Comment on the morphology of the red blood cells.
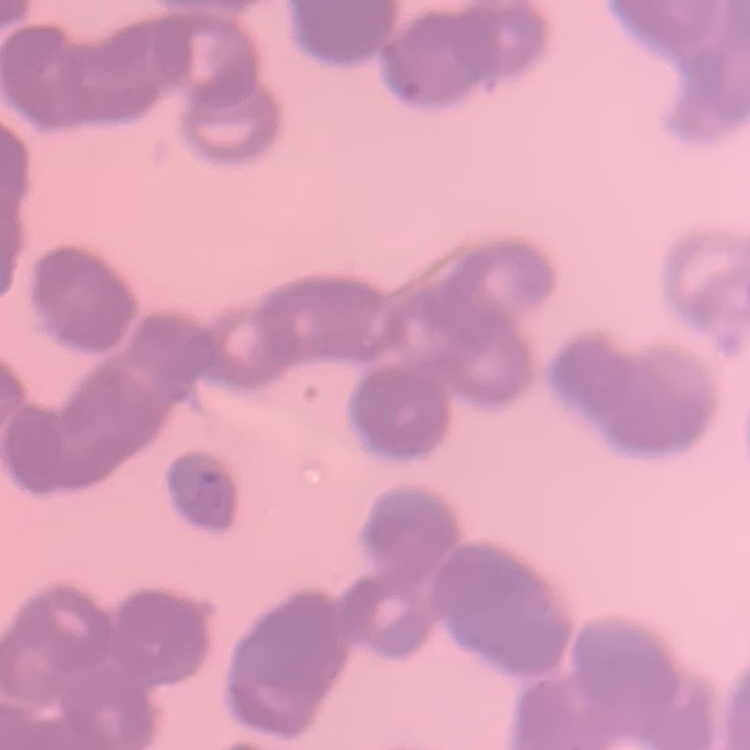
Rouleaux formation.

One tile cut from a larger photomicrograph. Stained with either Field's or Giemsa. Thin blood smear.